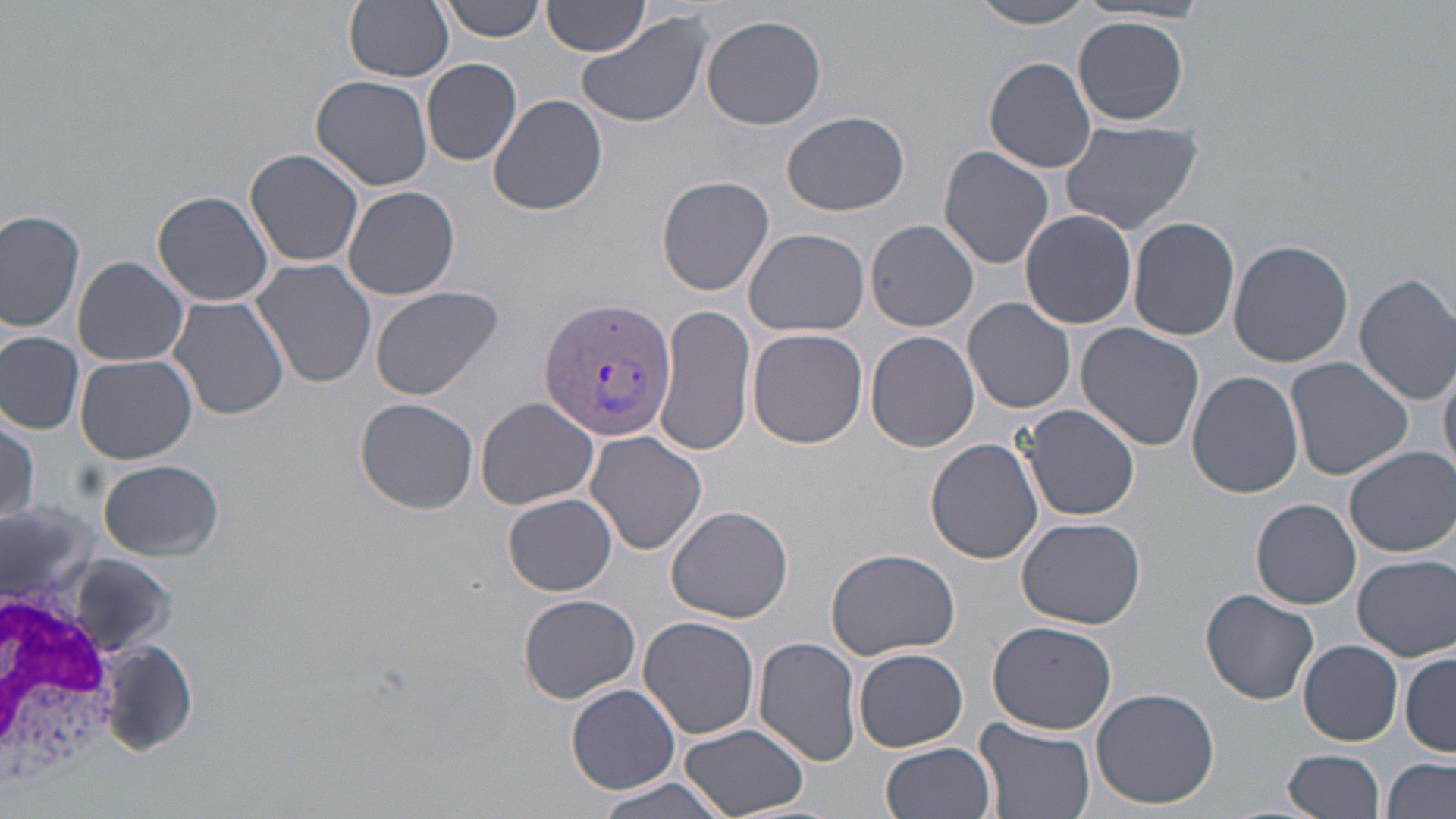

Summary:
  - Coordinate format: approximate bounding boxes as named x1/y1/x2/y2 corners in pixels
  - Uninfected red blood cell locations: (x1=345, y1=0, x2=454, y2=82), (x1=969, y1=0, x2=1098, y2=29), (x1=440, y1=1, x2=547, y2=42), (x1=543, y1=1, x2=650, y2=56), (x1=575, y1=10, x2=713, y2=128), (x1=702, y1=14, x2=827, y2=130), (x1=1074, y1=17, x2=1189, y2=125), (x1=984, y1=57, x2=1099, y2=172), (x1=422, y1=59, x2=522, y2=166), (x1=312, y1=73, x2=435, y2=191), (x1=487, y1=93, x2=608, y2=216), (x1=782, y1=111, x2=909, y2=216), (x1=1058, y1=121, x2=1203, y2=235), (x1=938, y1=147, x2=1055, y2=269), (x1=244, y1=148, x2=364, y2=269), (x1=656, y1=174, x2=775, y2=296), (x1=343, y1=184, x2=460, y2=300), (x1=153, y1=190, x2=275, y2=307), (x1=1020, y1=209, x2=1137, y2=329), (x1=0, y1=210, x2=85, y2=334), (x1=1129, y1=216, x2=1240, y2=342), (x1=866, y1=220, x2=980, y2=332), (x1=744, y1=229, x2=872, y2=337), (x1=1228, y1=239, x2=1352, y2=367), (x1=74, y1=255, x2=190, y2=366), (x1=251, y1=257, x2=377, y2=390), (x1=1354, y1=271, x2=1456, y2=404), (x1=368, y1=284, x2=505, y2=402), (x1=167, y1=297, x2=290, y2=424), (x1=964, y1=298, x2=1077, y2=415), (x1=659, y1=306, x2=757, y2=459), (x1=1076, y1=324, x2=1205, y2=450), (x1=748, y1=328, x2=869, y2=449), (x1=1, y1=331, x2=84, y2=434), (x1=865, y1=331, x2=979, y2=453), (x1=75, y1=355, x2=198, y2=463), (x1=1285, y1=357, x2=1414, y2=481), (x1=1439, y1=358, x2=1456, y2=478), (x1=1187, y1=371, x2=1304, y2=498), (x1=355, y1=397, x2=479, y2=513), (x1=476, y1=397, x2=600, y2=511), (x1=1020, y1=404, x2=1140, y2=521), (x1=0, y1=416, x2=41, y2=526), (x1=585, y1=431, x2=706, y2=556), (x1=926, y1=439, x2=1045, y2=564), (x1=1345, y1=447, x2=1454, y2=557), (x1=97, y1=459, x2=223, y2=561), (x1=503, y1=493, x2=618, y2=596), (x1=1250, y1=498, x2=1360, y2=610), (x1=666, y1=506, x2=794, y2=624), (x1=1017, y1=517, x2=1148, y2=628), (x1=826, y1=546, x2=960, y2=660), (x1=1352, y1=554, x2=1455, y2=662), (x1=63, y1=556, x2=177, y2=651), (x1=1201, y1=589, x2=1320, y2=704), (x1=519, y1=593, x2=641, y2=703), (x1=639, y1=615, x2=761, y2=740), (x1=986, y1=619, x2=1117, y2=734), (x1=753, y1=635, x2=862, y2=766), (x1=94, y1=639, x2=203, y2=757), (x1=1299, y1=640, x2=1403, y2=746), (x1=853, y1=648, x2=967, y2=751), (x1=1401, y1=652, x2=1456, y2=754), (x1=566, y1=684, x2=680, y2=792), (x1=1092, y1=687, x2=1219, y2=809), (x1=974, y1=719, x2=1097, y2=819), (x1=681, y1=725, x2=810, y2=817), (x1=881, y1=742, x2=997, y2=819), (x1=1283, y1=748, x2=1387, y2=819), (x1=1383, y1=757, x2=1455, y2=819), (x1=593, y1=775, x2=735, y2=819)
  - White blood cell locations: (x1=0, y1=580, x2=125, y2=801)
  - Plasmodium vivax-infected red blood cell locations: (x1=536, y1=295, x2=676, y2=440)
  - Slide-level diagnosis: Plasmodium vivax
  - Preparation: thin blood film
  - Stain: May-Grünwald-Giemsa
  - Magnification: 1000x
  - Image size: 1456×819 pixels
  - Field of view: one of a larger specimen
  - Modality: optical microscopy